Give the extent of all uninfected red blood cells.
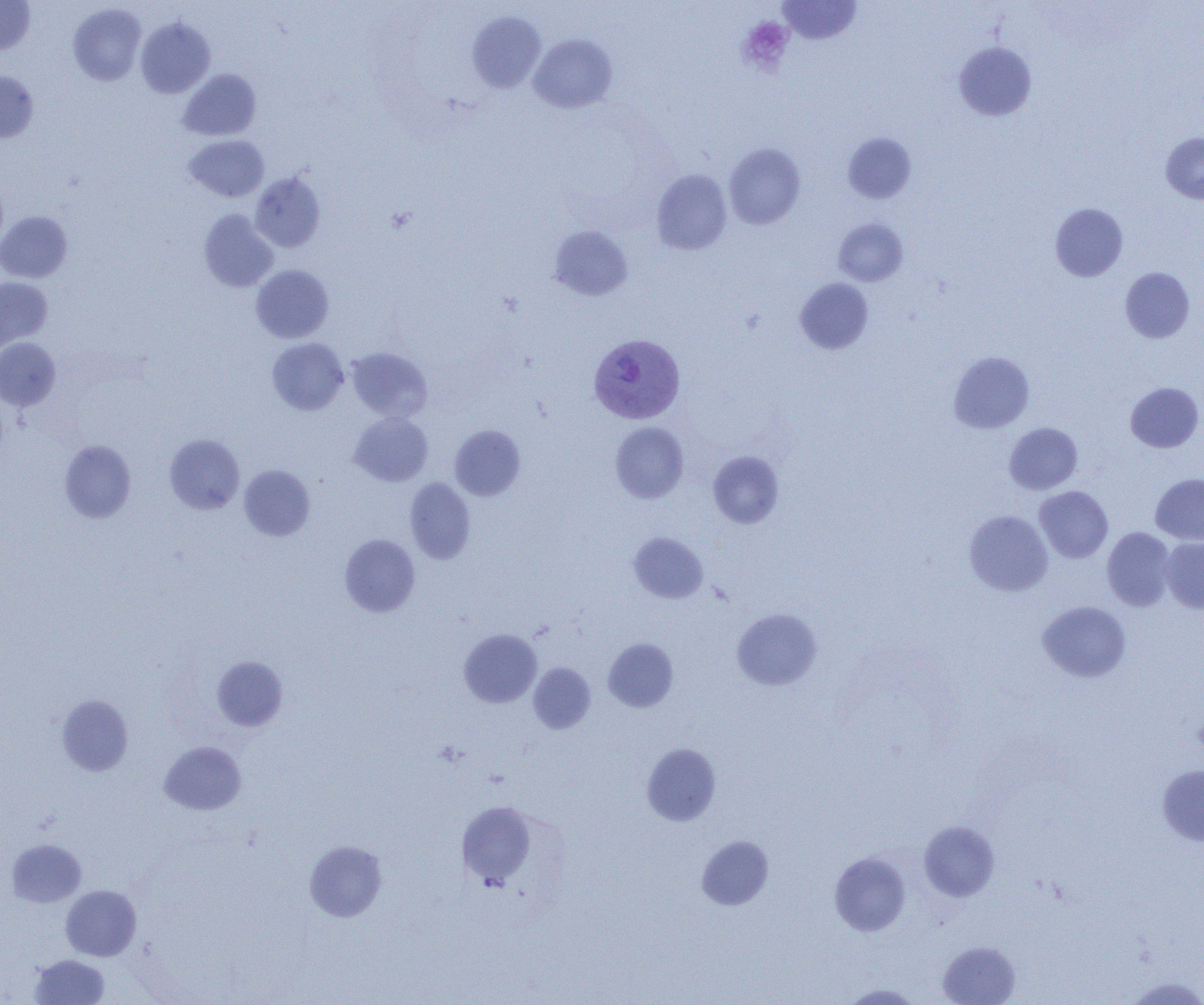
Approximate bounding boxes as [x1, y1, x2, y2] in pixels.
Uninfected red blood cells: [0, 0, 35, 54], [778, 1, 861, 45], [68, 3, 147, 85], [467, 11, 546, 93], [136, 17, 215, 98], [529, 34, 617, 113], [954, 42, 1037, 121], [178, 69, 261, 141], [0, 71, 39, 144], [842, 132, 916, 204], [1161, 132, 1204, 203], [184, 135, 269, 202], [724, 143, 806, 230], [651, 169, 732, 255], [250, 172, 326, 252], [1050, 203, 1128, 281], [199, 210, 278, 292], [0, 211, 72, 282], [833, 218, 908, 286], [549, 225, 634, 301], [251, 264, 333, 343], [1120, 267, 1195, 343], [0, 277, 53, 351], [795, 278, 873, 354], [0, 337, 60, 410], [267, 338, 349, 415], [347, 347, 432, 422], [948, 351, 1035, 433], [1125, 382, 1203, 453], [349, 412, 433, 487], [610, 422, 688, 503], [1004, 422, 1083, 494], [450, 425, 525, 500], [164, 434, 245, 514], [59, 440, 136, 523], [708, 451, 785, 528], [239, 464, 315, 541], [1150, 473, 1204, 545], [405, 478, 475, 563], [1034, 486, 1113, 563], [964, 510, 1053, 596], [1102, 527, 1176, 611], [629, 532, 708, 603], [339, 534, 420, 617], [1160, 537, 1204, 613], [1037, 601, 1131, 682], [732, 608, 822, 690], [459, 629, 541, 708], [603, 638, 678, 712], [212, 656, 287, 731], [528, 662, 595, 733], [56, 694, 134, 776], [159, 741, 246, 815], [642, 742, 721, 826], [1157, 765, 1204, 845], [456, 800, 538, 888], [919, 820, 1000, 901], [697, 835, 773, 910], [6, 839, 86, 907], [304, 840, 388, 921], [830, 852, 910, 936], [61, 885, 141, 961], [937, 941, 1021, 1005], [30, 954, 110, 1004], [1123, 976, 1204, 1005], [840, 983, 924, 1004].

Platelet locations: [737, 17, 794, 75]. Plasmodium vivax-infected red blood cell locations: [589, 333, 684, 424]. Slide-level diagnosis: Plasmodium vivax. Thin blood smear. One field of a larger specimen. 1000x magnification. Image is 1204×1005 pixels. Light microscopy.